Report the malaria status of this cell.
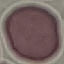

It is uninfected.

image type = automatically extracted cell patch, resized to 64 × 64 pixels
stain = Giemsa
preparation = thin smear
capture = smartphone through the microscope eyepiece